State the blood parasite species.
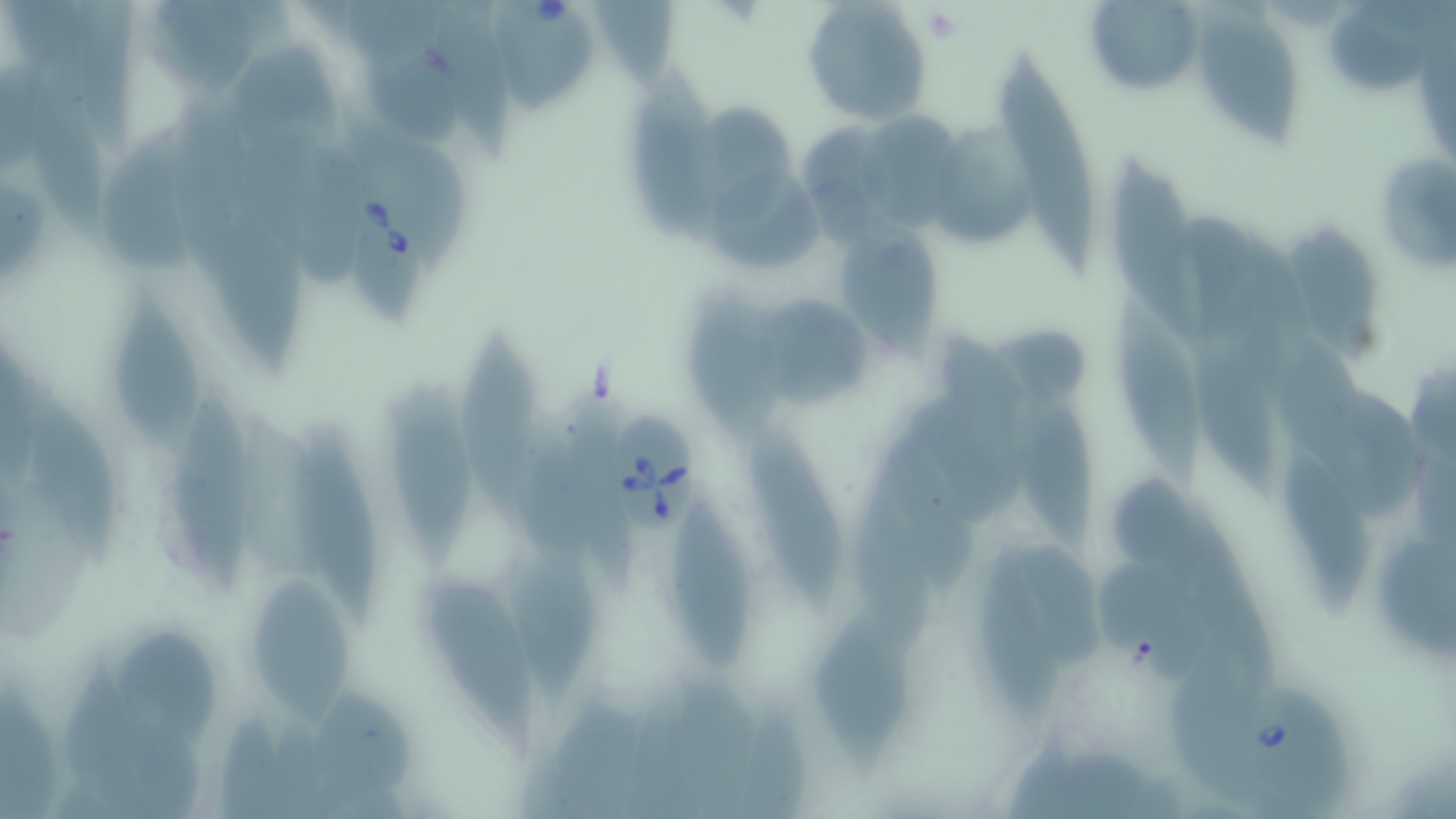
Babesia divergens.

Approximate bounding boxes as [x1, y1, x2, y2] in pixels. Platelet locations: [919, 7, 963, 42]. Uninfected red blood cell locations: [799, 0, 931, 128], [1084, 0, 1206, 99], [1329, 3, 1441, 97], [1202, 15, 1302, 148], [367, 45, 465, 150], [997, 54, 1098, 275], [27, 69, 119, 251], [630, 71, 725, 242], [703, 109, 797, 224], [862, 114, 970, 233], [936, 125, 1035, 244], [103, 128, 200, 273], [1371, 151, 1456, 273], [1111, 156, 1207, 348], [217, 194, 312, 373], [839, 217, 944, 358], [1291, 228, 1382, 360], [686, 283, 775, 447], [1104, 286, 1204, 491], [110, 293, 207, 460], [763, 297, 875, 412], [460, 326, 545, 526], [1194, 340, 1276, 494], [1015, 387, 1100, 553], [386, 388, 477, 564], [168, 394, 255, 592], [27, 396, 120, 569], [294, 428, 380, 624], [751, 435, 845, 612], [890, 443, 979, 601], [1283, 447, 1373, 608], [673, 503, 754, 672], [1376, 543, 1456, 664], [516, 554, 601, 703], [979, 557, 1066, 717], [418, 571, 543, 744], [251, 579, 355, 727], [814, 616, 915, 777], [113, 633, 226, 748], [312, 692, 415, 809]. Babesia divergens-infected red blood cell locations: [485, 0, 610, 118], [340, 171, 433, 327], [606, 408, 701, 542], [1241, 675, 1354, 813]. One field of a larger specimen. May-Grünwald-Giemsa-stained preparation. Image is 1456×819 pixels. Captured at 1000x magnification. Thin blood smear. Light microscopy.